Classify this cell by malaria status.
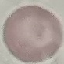
It is uninfected.

Cell patch, automatically extracted from a larger field of view and resized to 64 × 64 pixels. Giemsa stain. Acquired by smartphone through the microscope eyepiece. Thin smear of blood.